Report the malaria status of this cell.
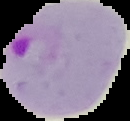

Parasitized.

preparation = thin blood smear
image size = 130×121 pixels
image type = cell region segmented out of the field of view; surrounding area masked to black